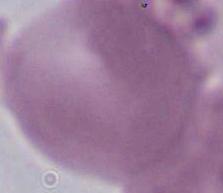
1000x magnification. A red blood cell is shown. Photomicrograph.